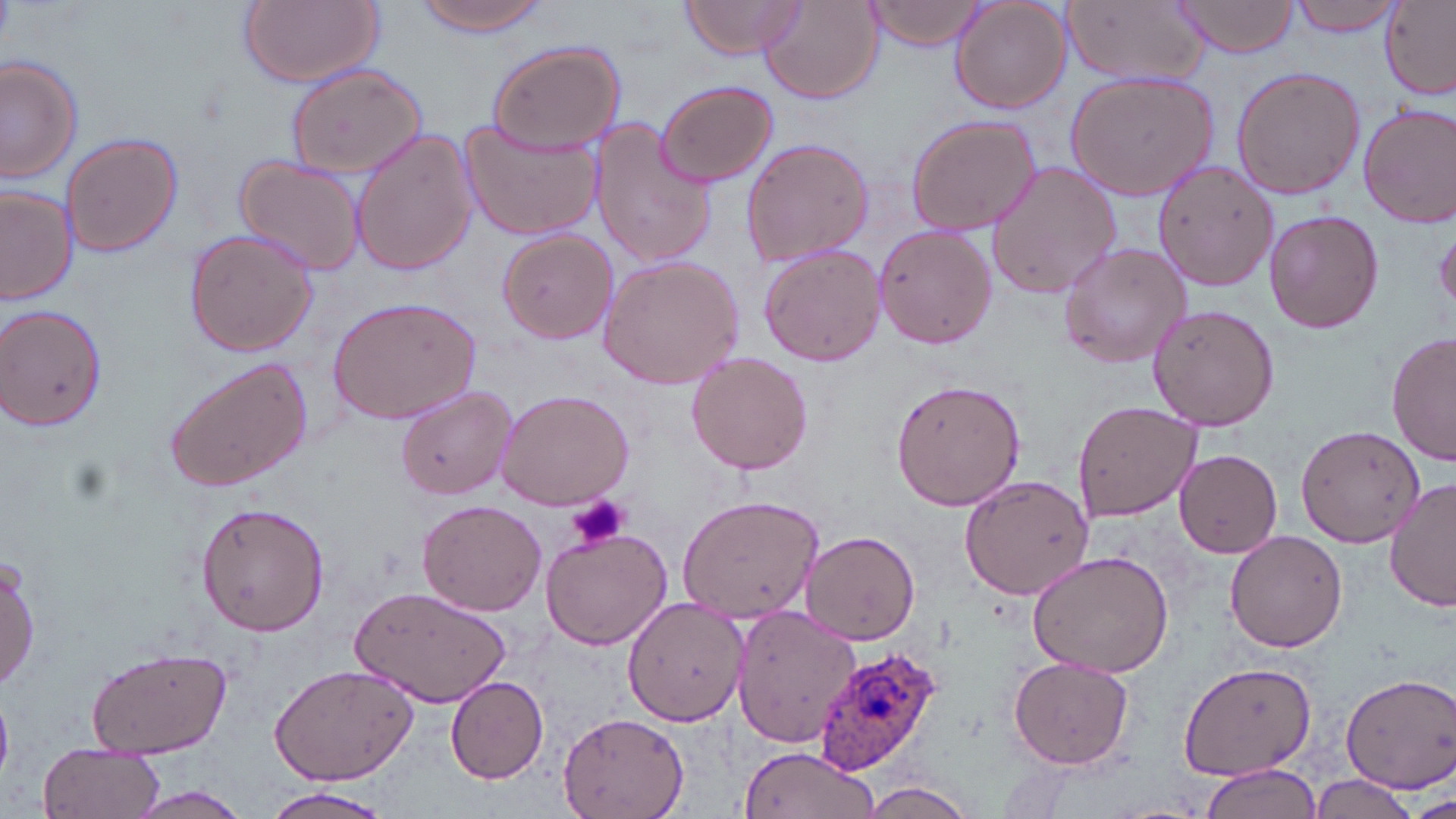
Summary:
  - Coordinate format: approximate bounding boxes as named x1/y1/x2/y2 corners in pixels
  - Platelet locations: (x1=569, y1=495, x2=631, y2=554)
  - Plasmodium ovale-infected red blood cell locations: (x1=812, y1=646, x2=943, y2=776)
  - Uninfected red blood cell locations: (x1=236, y1=0, x2=384, y2=88), (x1=414, y1=0, x2=555, y2=37), (x1=678, y1=0, x2=806, y2=59), (x1=1173, y1=0, x2=1302, y2=60), (x1=1287, y1=0, x2=1404, y2=33), (x1=866, y1=1, x2=988, y2=51), (x1=949, y1=1, x2=1070, y2=115), (x1=1062, y1=1, x2=1207, y2=87), (x1=758, y1=2, x2=883, y2=106), (x1=1377, y1=2, x2=1455, y2=100), (x1=486, y1=41, x2=625, y2=153), (x1=0, y1=54, x2=82, y2=186), (x1=282, y1=63, x2=428, y2=180), (x1=1230, y1=65, x2=1365, y2=200), (x1=1064, y1=71, x2=1218, y2=201), (x1=654, y1=79, x2=778, y2=188), (x1=1357, y1=102, x2=1456, y2=228), (x1=904, y1=113, x2=1043, y2=235), (x1=457, y1=118, x2=603, y2=242), (x1=588, y1=120, x2=717, y2=271), (x1=349, y1=128, x2=478, y2=277), (x1=60, y1=132, x2=183, y2=258), (x1=739, y1=135, x2=875, y2=270), (x1=235, y1=156, x2=365, y2=278), (x1=1154, y1=159, x2=1281, y2=294), (x1=984, y1=160, x2=1121, y2=300), (x1=1, y1=183, x2=76, y2=304), (x1=1263, y1=210, x2=1383, y2=333), (x1=873, y1=224, x2=996, y2=352), (x1=1434, y1=225, x2=1455, y2=319), (x1=181, y1=226, x2=320, y2=357), (x1=496, y1=229, x2=619, y2=344), (x1=1055, y1=242, x2=1192, y2=370), (x1=757, y1=243, x2=886, y2=368), (x1=596, y1=254, x2=746, y2=392), (x1=326, y1=296, x2=482, y2=428), (x1=1, y1=302, x2=109, y2=431), (x1=1146, y1=302, x2=1281, y2=431), (x1=1387, y1=332, x2=1455, y2=469), (x1=686, y1=352, x2=813, y2=475), (x1=162, y1=356, x2=312, y2=493), (x1=888, y1=375, x2=1027, y2=510), (x1=395, y1=385, x2=518, y2=500), (x1=494, y1=387, x2=635, y2=511), (x1=1072, y1=397, x2=1203, y2=522), (x1=1295, y1=423, x2=1426, y2=546), (x1=1173, y1=448, x2=1283, y2=559), (x1=958, y1=474, x2=1097, y2=600), (x1=1386, y1=478, x2=1455, y2=614), (x1=677, y1=495, x2=823, y2=624), (x1=417, y1=498, x2=548, y2=616), (x1=197, y1=500, x2=330, y2=636), (x1=538, y1=523, x2=675, y2=649), (x1=802, y1=530, x2=921, y2=645), (x1=1226, y1=530, x2=1348, y2=654), (x1=1025, y1=549, x2=1177, y2=681), (x1=1, y1=554, x2=40, y2=692), (x1=350, y1=587, x2=512, y2=710), (x1=622, y1=595, x2=748, y2=725), (x1=731, y1=606, x2=860, y2=747), (x1=85, y1=646, x2=232, y2=758), (x1=1008, y1=656, x2=1135, y2=769), (x1=1177, y1=661, x2=1315, y2=784), (x1=269, y1=663, x2=420, y2=785), (x1=1339, y1=673, x2=1456, y2=792), (x1=445, y1=676, x2=549, y2=782), (x1=558, y1=711, x2=688, y2=817), (x1=39, y1=741, x2=164, y2=819), (x1=735, y1=745, x2=878, y2=818), (x1=1197, y1=762, x2=1320, y2=819), (x1=1308, y1=774, x2=1422, y2=817), (x1=861, y1=781, x2=979, y2=818), (x1=123, y1=785, x2=256, y2=819), (x1=260, y1=791, x2=396, y2=819), (x1=1409, y1=795, x2=1455, y2=819)
  - Slide-level diagnosis: Plasmodium ovale
  - Preparation: thin blood smear
  - Stain: May-Grünwald-Giemsa
  - Image size: 1456×819 pixels
  - Modality: optical microscopy
  - Field of view: one of a larger specimen
  - Magnification: 1000x